Outline platelets.
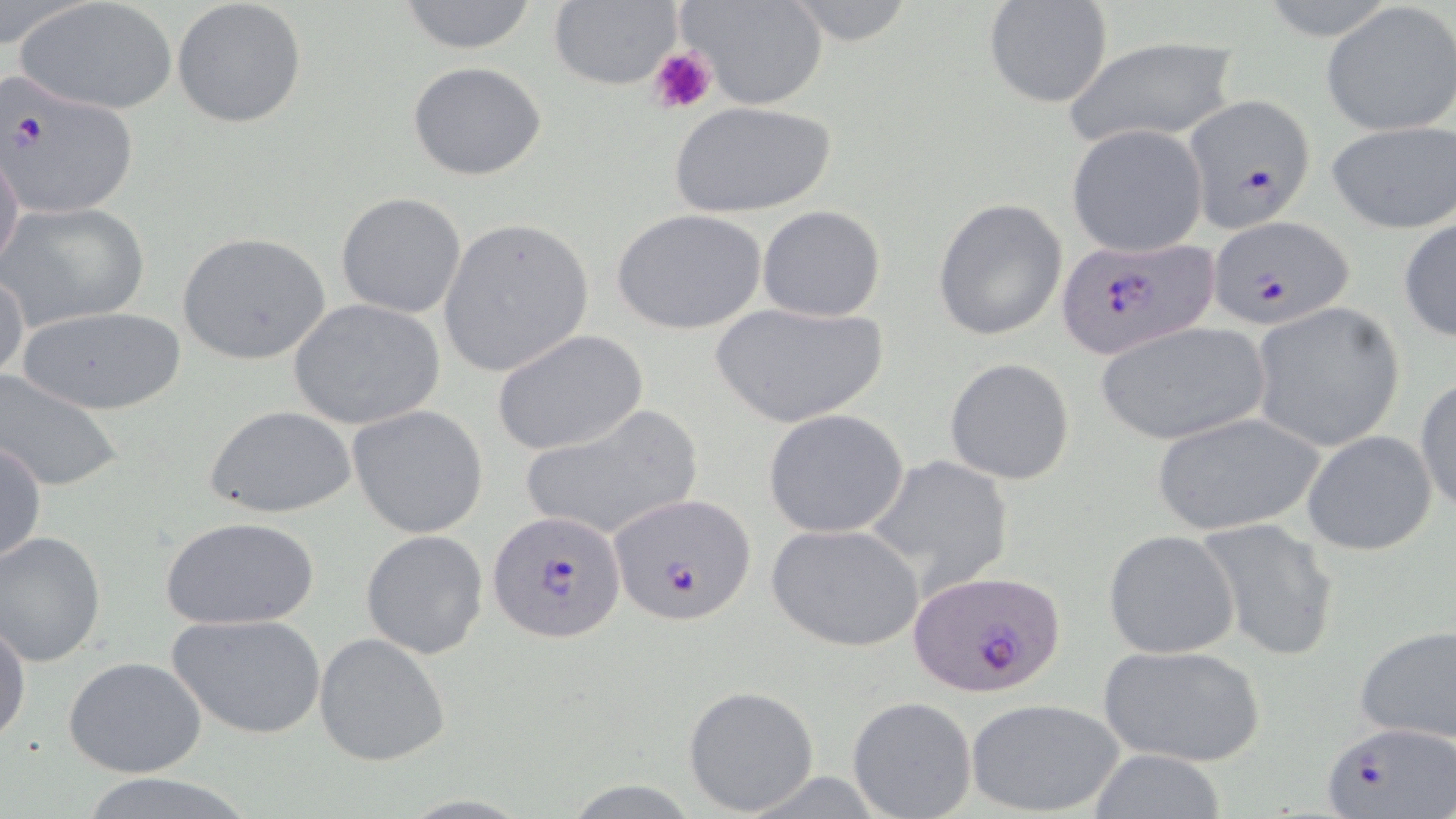
Approximate bounding boxes as named x1/y1/x2/y2 corners in pixels.
Platelets: (x1=648, y1=47, x2=715, y2=114).

Summary:
  - Plasmodium falciparum-infected red blood cell locations: (x1=2, y1=75, x2=140, y2=220), (x1=1184, y1=93, x2=1316, y2=227), (x1=1209, y1=215, x2=1355, y2=331), (x1=1055, y1=236, x2=1220, y2=361), (x1=607, y1=493, x2=759, y2=625), (x1=488, y1=509, x2=627, y2=644), (x1=911, y1=569, x2=1065, y2=697), (x1=1324, y1=722, x2=1455, y2=816)
  - Uninfected red blood cell locations: (x1=172, y1=0, x2=308, y2=130), (x1=392, y1=0, x2=545, y2=54), (x1=676, y1=0, x2=829, y2=110), (x1=780, y1=0, x2=920, y2=48), (x1=15, y1=1, x2=179, y2=115), (x1=546, y1=1, x2=683, y2=90), (x1=981, y1=2, x2=1114, y2=109), (x1=1321, y1=2, x2=1456, y2=135), (x1=1063, y1=36, x2=1242, y2=145), (x1=407, y1=60, x2=548, y2=182), (x1=671, y1=100, x2=838, y2=220), (x1=1324, y1=120, x2=1455, y2=235), (x1=1066, y1=125, x2=1209, y2=258), (x1=0, y1=145, x2=25, y2=274), (x1=336, y1=192, x2=469, y2=319), (x1=932, y1=197, x2=1067, y2=341), (x1=2, y1=200, x2=151, y2=332), (x1=757, y1=205, x2=887, y2=322), (x1=611, y1=208, x2=771, y2=337), (x1=1397, y1=214, x2=1455, y2=344), (x1=436, y1=216, x2=595, y2=378), (x1=177, y1=232, x2=331, y2=364), (x1=1, y1=269, x2=28, y2=386), (x1=287, y1=297, x2=445, y2=429), (x1=710, y1=300, x2=890, y2=428), (x1=1251, y1=302, x2=1405, y2=454), (x1=12, y1=305, x2=189, y2=416), (x1=1094, y1=322, x2=1271, y2=446), (x1=492, y1=328, x2=648, y2=456), (x1=943, y1=357, x2=1075, y2=485), (x1=0, y1=368, x2=125, y2=492), (x1=1413, y1=373, x2=1456, y2=515), (x1=204, y1=404, x2=356, y2=519), (x1=348, y1=405, x2=491, y2=539), (x1=516, y1=405, x2=706, y2=541), (x1=763, y1=408, x2=913, y2=539), (x1=1151, y1=409, x2=1327, y2=535), (x1=1302, y1=429, x2=1438, y2=556), (x1=1, y1=439, x2=47, y2=567), (x1=863, y1=454, x2=1017, y2=594), (x1=160, y1=515, x2=321, y2=630), (x1=1193, y1=517, x2=1341, y2=661), (x1=766, y1=522, x2=925, y2=652), (x1=360, y1=529, x2=489, y2=658), (x1=1103, y1=530, x2=1240, y2=660), (x1=0, y1=531, x2=106, y2=667), (x1=168, y1=612, x2=326, y2=740), (x1=0, y1=617, x2=29, y2=746), (x1=1353, y1=626, x2=1456, y2=745), (x1=314, y1=632, x2=451, y2=767), (x1=1098, y1=643, x2=1266, y2=767), (x1=64, y1=655, x2=206, y2=779), (x1=683, y1=685, x2=820, y2=815), (x1=847, y1=695, x2=977, y2=819), (x1=967, y1=698, x2=1125, y2=817), (x1=1084, y1=749, x2=1229, y2=818), (x1=74, y1=772, x2=258, y2=819)
  - Slide-level diagnosis: Plasmodium falciparum
  - Stain: May-Grünwald-Giemsa
  - Modality: light microscopy
  - Image size: 1456×819 pixels
  - Preparation: thin blood smear
  - Magnification: 1000x
  - Field of view: single